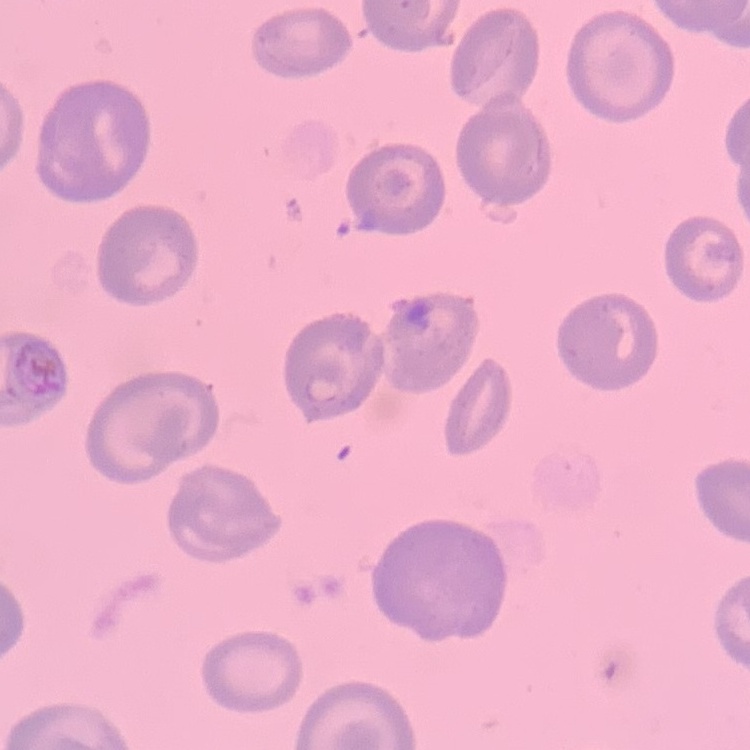

The red blood cells exhibit no rouleaux formation. Stained with either Field's or Giemsa. Thin blood smear. Square crop of a larger photomicrograph.